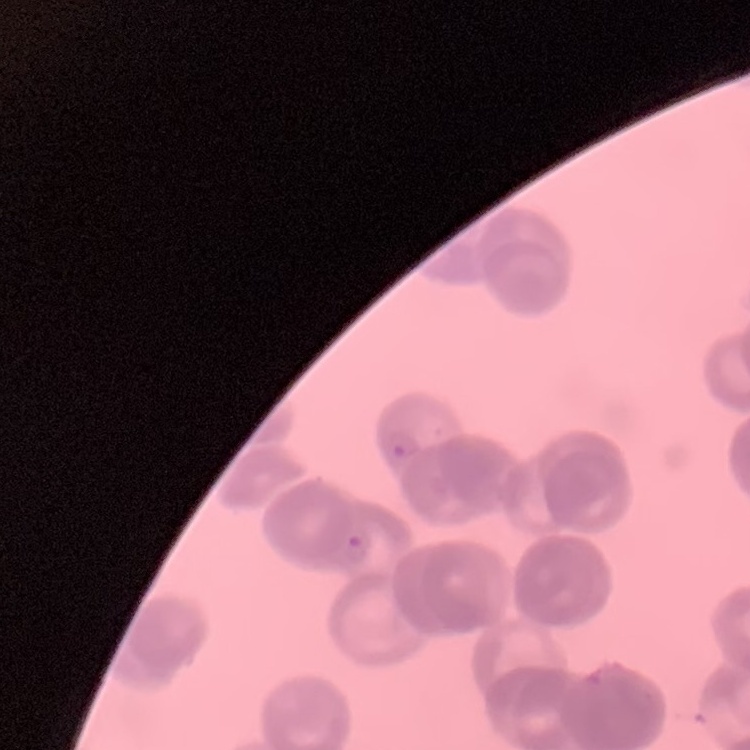

Summary:
  - Erythrocyte morphology: rouleaux formation
  - Image type: square crop of a larger photomicrograph
  - Preparation: thin blood smear
  - Stain: Field's or Giemsa